Describe the morphology of the red blood cells.
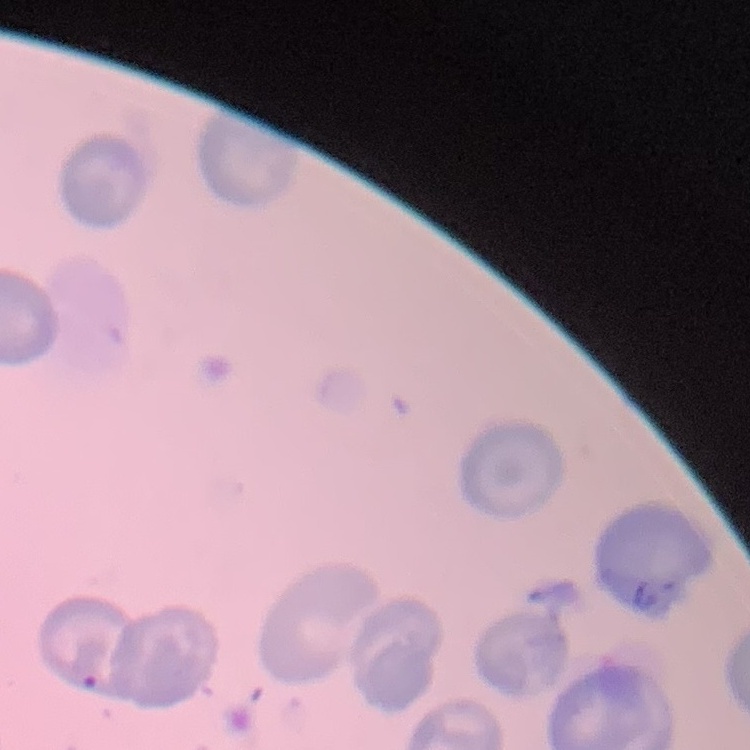

No rouleaux formation.

Thin blood smear. One tile cut from a larger photomicrograph. Field's or Giemsa stain.